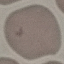 Result: negative for malaria parasites. Thin smear of blood. Acquired by smartphone through the microscope eyepiece. Cell patch, automatically extracted from a larger field of view and resized to 64 × 64 pixels. Giemsa stain.